Describe the morphology of the erythrocytes.
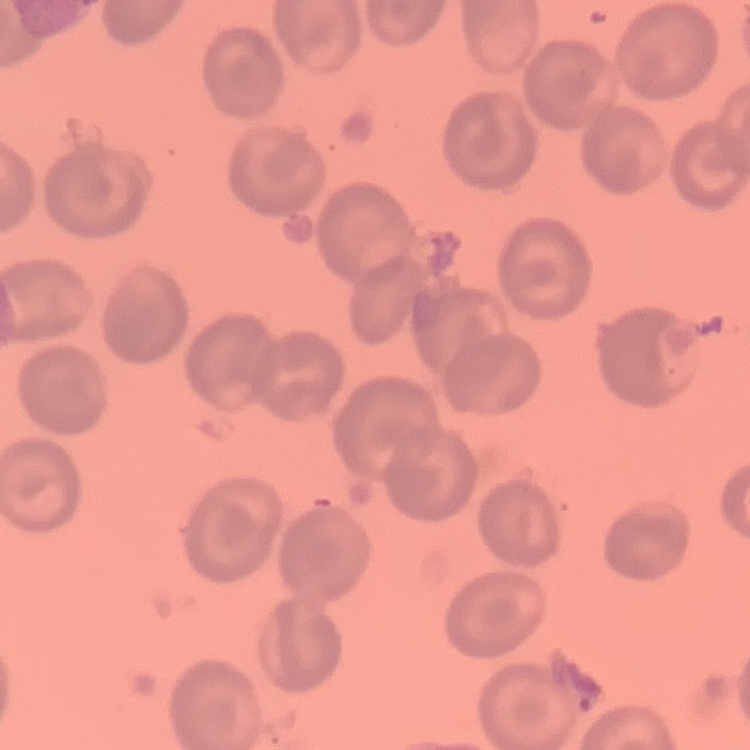
No rouleaux formation.

Thin blood smear. Square crop of a larger photomicrograph. Field's or Giemsa stain.